Classify this cell by malaria status.
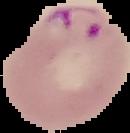
It is parasitized.

image size = 130×133 pixels
preparation = thin blood smear
image type = segmented cell region on a black background